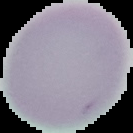 From a thin blood film. The area outside the segmented cell region is set to black. Result: negative for malaria parasites. Image is 133×133 pixels.